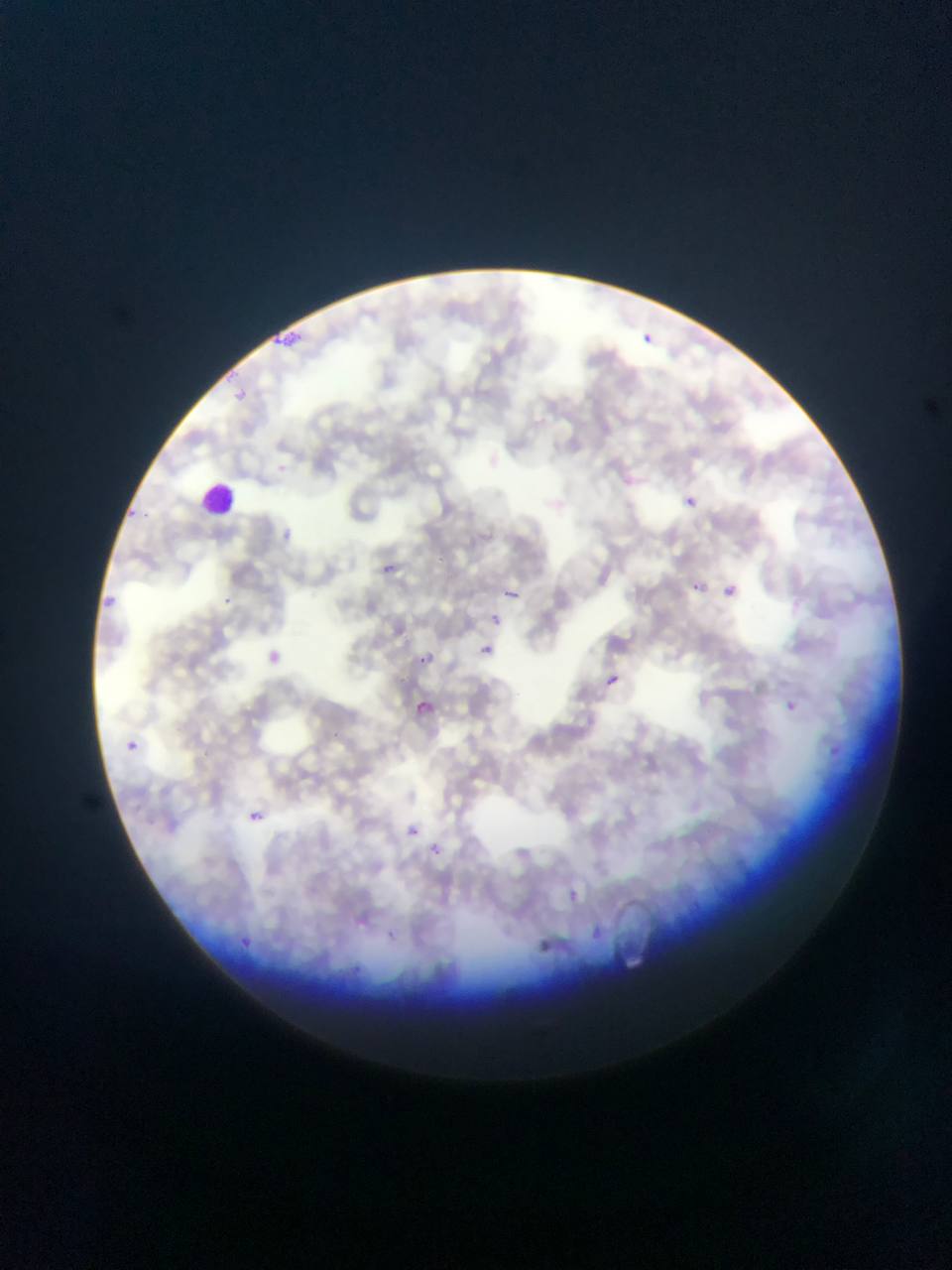
Approximate bounding boxes as left top right bottom in pixels. Plasmodium parasite locations: 271 328 292 356; 641 332 654 345; 289 333 300 343; 232 388 253 409; 619 472 636 489; 683 493 699 508; 126 504 140 519; 283 525 300 548; 383 561 396 580; 690 581 702 593; 100 583 128 610; 723 584 737 598; 505 588 518 600; 218 594 238 617; 490 613 502 626; 481 642 498 657; 268 643 296 679; 415 652 429 664; 605 675 619 687; 784 695 800 707; 419 701 437 713; 126 741 140 754; 830 741 840 758; 249 803 267 820; 406 821 425 833; 431 844 442 856; 563 889 584 902; 594 925 611 941; 235 931 257 958; 537 931 556 948. Leukocyte locations: 200 484 241 516. Sample from Ghana. One field of view. Photographed through a microscope with a mobile-phone camera. Image is 952×1270 pixels. Thin blood smear.